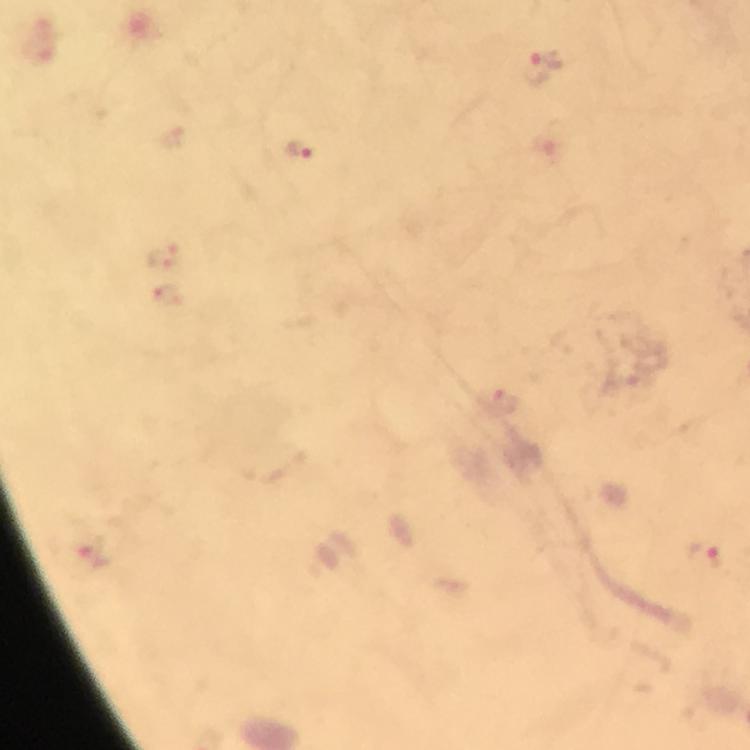

Approximate centers as (x, y) in pixels.
Summary:
  - Malaria parasite locations: (543, 66), (301, 151), (161, 254), (167, 296), (498, 400), (706, 555)
  - Preparation: thick smear
  - Immersion oil: applied
  - Magnification: 100x
  - Context: from a diagnostic examination for malaria
  - Image size: 750×750 pixels
  - Cropped from: one field of view
  - Capture: smartphone mounted on the microscope
  - Stain: Giemsa